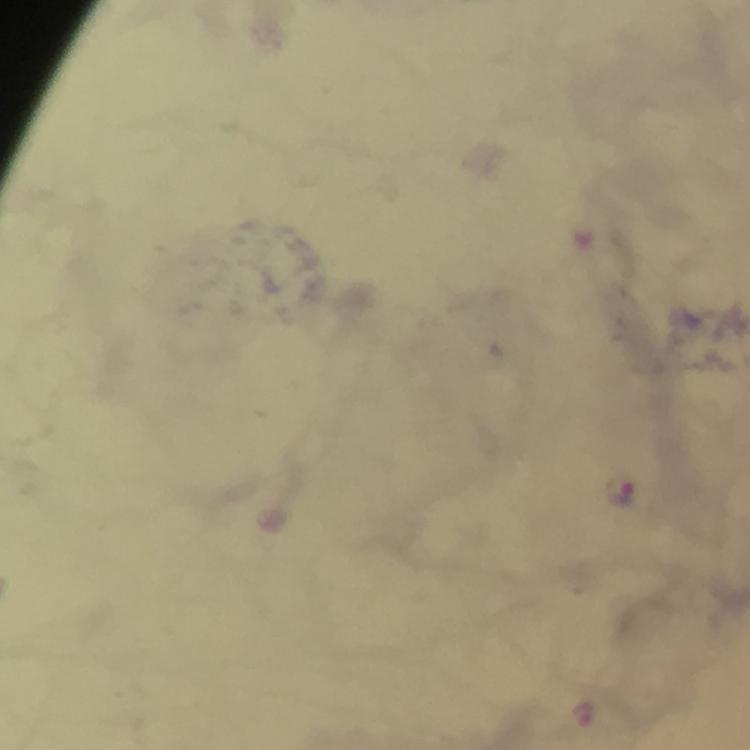
Approximate object centers, in pixels from the top-left corner. Plasmodium parasite locations: (x=623, y=493), (x=584, y=713). From a malaria diagnostic workup. Image is 750×750 pixels. Photographed through the microscope with a smartphone camera. Immersion oil applied. Cropped region of a single field of view. At 100x magnification. Thick blood film. Giemsa stain.